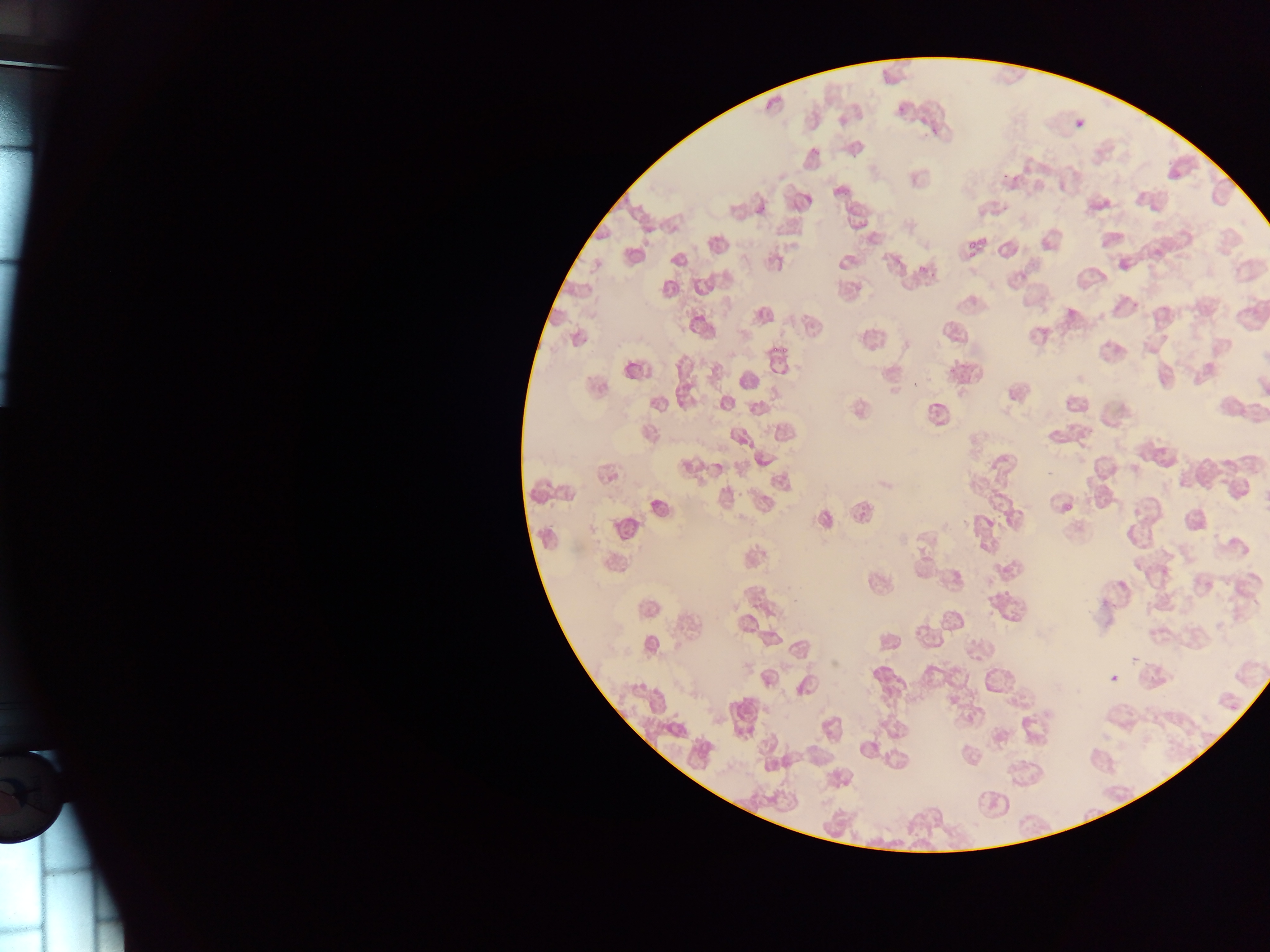

Approximate bounding boxes as {left, top, right, bottom} in pixels.
Summary:
  - Plasmodium parasite locations (subset; some below the resolvable size): {895, 106, 904, 115}, {1076, 120, 1083, 128}, {622, 525, 633, 537}, {1110, 675, 1119, 683}
  - Image size: 1270×952 pixels
  - Country: Ghana
  - Preparation: thin blood film
  - Field of view: single
  - Capture: mobile-phone photograph through a microscope